Identify the cell.
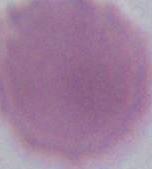
An erythrocyte.

Micrograph. 1000x magnification.